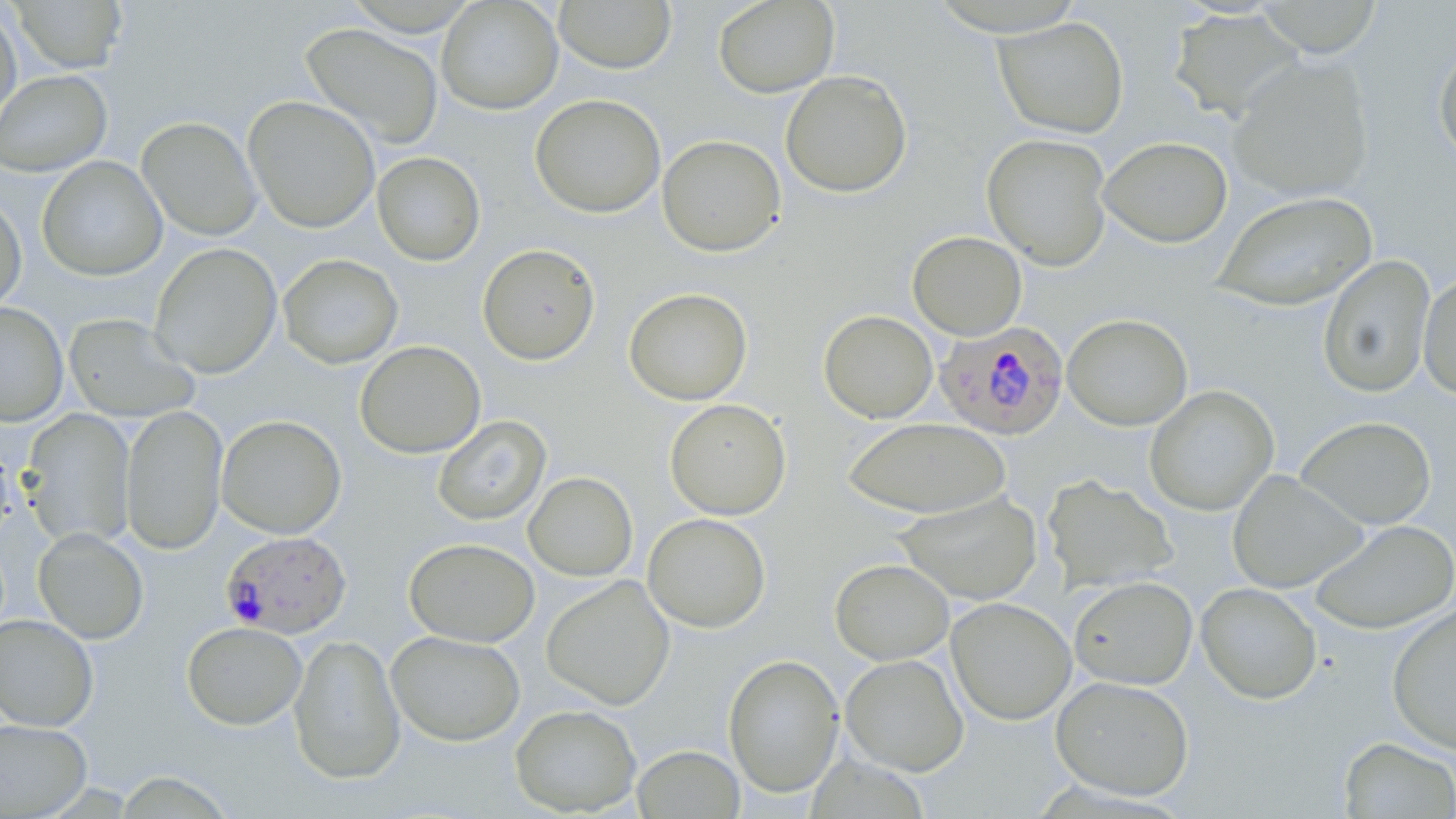
Summary:
  - Coordinate format: approximate bounding boxes as (x1, y1, x2, y2) in pixels
  - Uninfected red blood cell locations: (436, 0, 563, 115), (553, 0, 677, 74), (712, 0, 839, 98), (10, 1, 128, 73), (1255, 1, 1383, 57), (0, 3, 22, 135), (1169, 8, 1305, 122), (994, 17, 1129, 138), (300, 22, 444, 149), (1434, 39, 1456, 166), (1228, 56, 1374, 201), (0, 69, 112, 176), (780, 70, 913, 197), (530, 94, 666, 218), (242, 95, 380, 234), (137, 116, 262, 241), (981, 133, 1113, 271), (657, 134, 786, 257), (1099, 136, 1232, 248), (372, 152, 486, 266), (36, 157, 167, 281), (1212, 190, 1377, 312), (0, 193, 27, 314), (907, 231, 1027, 340), (149, 243, 282, 379), (477, 243, 600, 365), (278, 254, 403, 369), (1317, 254, 1436, 398), (1418, 271, 1456, 401), (623, 287, 752, 405), (0, 301, 69, 427), (818, 309, 938, 423), (63, 313, 200, 423), (1062, 313, 1192, 431), (354, 340, 486, 458), (1144, 385, 1279, 516), (664, 398, 791, 520), (120, 404, 228, 555), (19, 409, 137, 549), (216, 414, 347, 539), (433, 415, 551, 525), (1296, 416, 1437, 530), (843, 417, 1011, 519), (0, 433, 18, 548), (1226, 470, 1367, 593), (523, 471, 638, 581), (1042, 474, 1179, 594), (895, 491, 1043, 606), (642, 513, 771, 632), (1308, 520, 1456, 634), (33, 528, 149, 644), (404, 537, 540, 647), (829, 558, 954, 664), (541, 575, 675, 710), (1069, 576, 1198, 690), (1196, 582, 1322, 704), (946, 597, 1076, 725), (1387, 603, 1456, 754), (0, 614, 99, 731), (182, 621, 307, 730), (385, 630, 525, 746), (288, 633, 406, 785), (723, 653, 844, 797), (841, 654, 968, 776), (1051, 675, 1194, 801), (510, 703, 642, 816), (0, 718, 92, 817), (1338, 737, 1455, 818), (632, 745, 744, 818)
  - Plasmodium falciparum-infected red blood cell locations: (934, 321, 1069, 441), (220, 530, 352, 639)
  - Slide-level diagnosis: Plasmodium falciparum
  - Field of view: single
  - Preparation: thin blood film
  - Modality: light microscopy
  - Image size: 1456×819 pixels
  - Stain: May-Grünwald-Giemsa
  - Magnification: 1000x